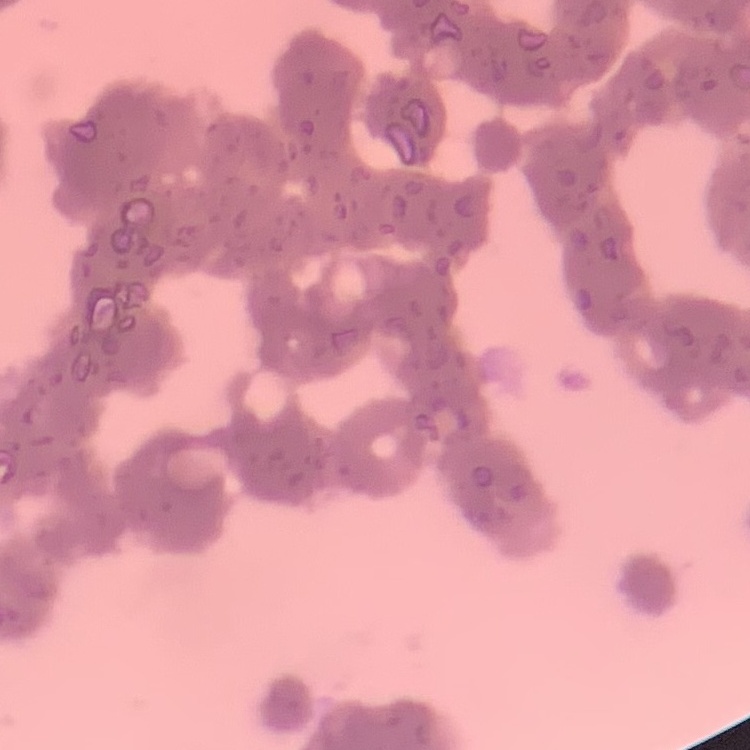

Summary:
  - Erythrocyte morphology: rouleaux formation
  - Image type: one tile cut from a larger photomicrograph
  - Preparation: thin peripheral smear
  - Stain: Field's or Giemsa